Outline each blood parasite and name the species.
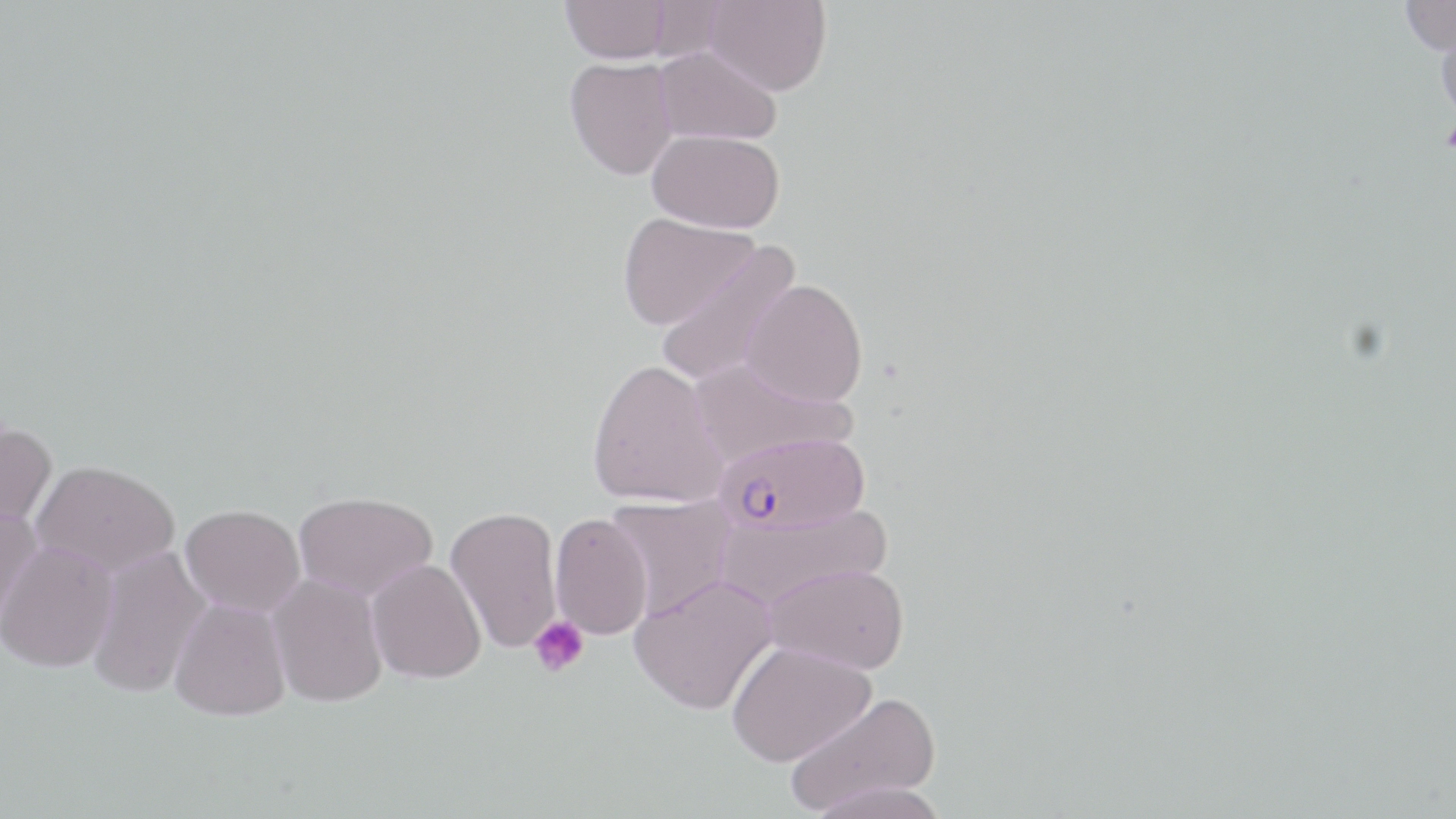

Approximate bounding boxes as [x1, y1, x2, y2] in pixels.
Plasmodium falciparum-infected red blood cells: [721, 433, 870, 535].
No Plasmodium ovale, Plasmodium malariae, Plasmodium vivax, Babesia divergens, or Trypanosoma brucei observed.

Platelet locations: [529, 616, 590, 679]. Uninfected red blood cell locations: [703, 0, 832, 96], [1399, 0, 1456, 56], [560, 1, 675, 64], [1435, 18, 1456, 127], [654, 45, 782, 146], [565, 57, 678, 180], [648, 129, 785, 233], [617, 212, 759, 329], [654, 240, 802, 387], [742, 278, 868, 407], [690, 357, 858, 467], [587, 358, 728, 508], [0, 420, 56, 537], [31, 460, 179, 577], [293, 491, 438, 602], [605, 494, 737, 620], [180, 504, 306, 618], [0, 506, 44, 633], [446, 506, 562, 653], [716, 507, 893, 611], [550, 512, 653, 639], [0, 540, 118, 672], [86, 545, 211, 699], [366, 558, 487, 683], [767, 562, 910, 674], [267, 573, 388, 708], [630, 573, 778, 714], [169, 598, 291, 721], [726, 640, 875, 767], [784, 691, 943, 816]. Slide-level diagnosis: Plasmodium falciparum. May-Grünwald-Giemsa-stained preparation. Captured at 1000x magnification. Thin blood smear. Image is 1456×819 pixels. One field of a larger specimen. Light microscopy.